Identify the cell.
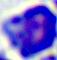

A leukocyte.

Micrograph. Captured at 400x magnification.